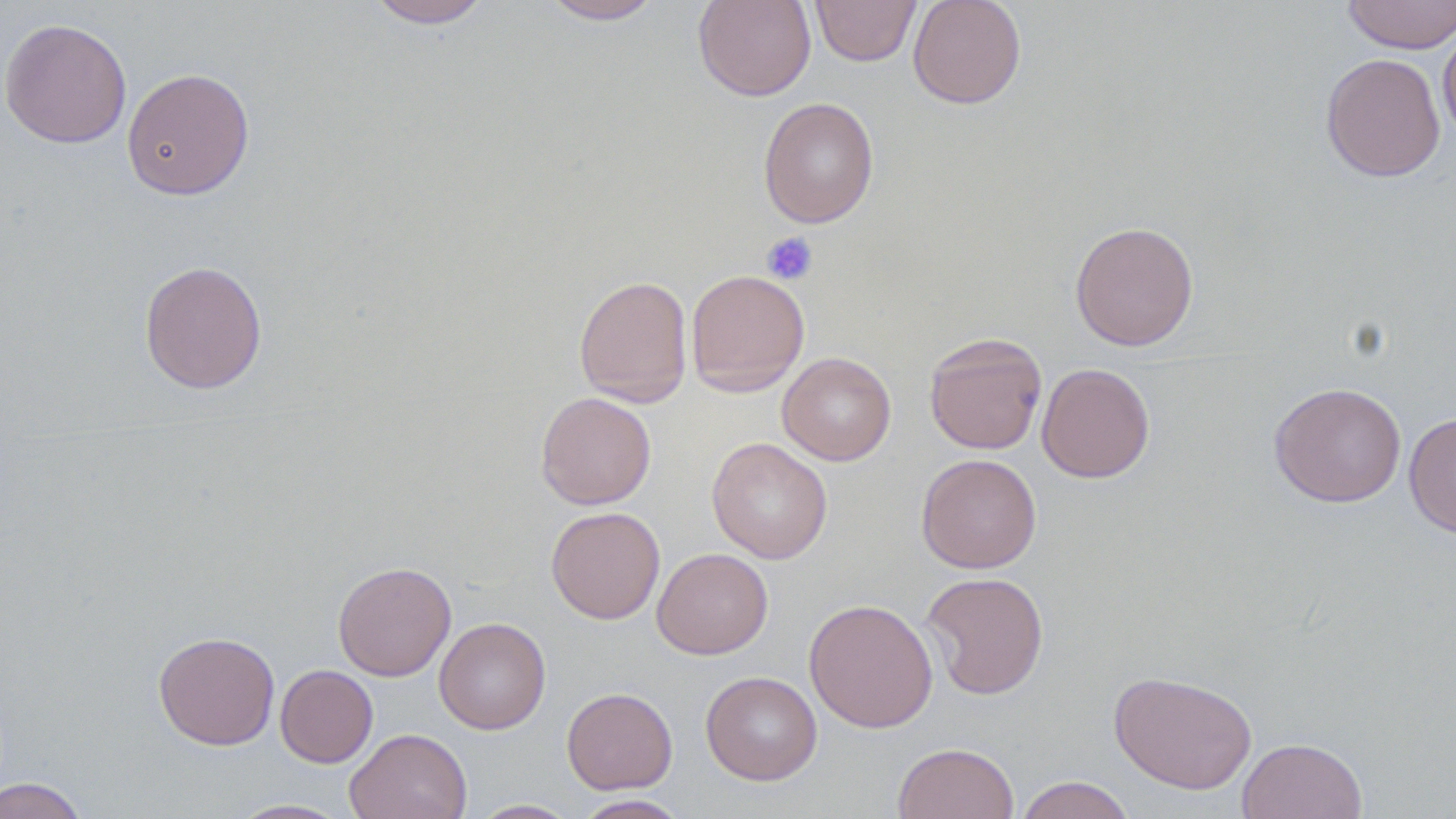 Approximate bounding boxes as named x1/y1/x2/y2 corners in pixels. Uninfected red blood cell locations: (x1=365, y1=0, x2=494, y2=28), (x1=540, y1=0, x2=665, y2=24), (x1=693, y1=0, x2=816, y2=101), (x1=810, y1=0, x2=921, y2=66), (x1=907, y1=0, x2=1027, y2=109), (x1=1341, y1=0, x2=1456, y2=54), (x1=0, y1=17, x2=132, y2=149), (x1=1438, y1=24, x2=1456, y2=144), (x1=1321, y1=52, x2=1446, y2=182), (x1=121, y1=67, x2=255, y2=200), (x1=758, y1=97, x2=879, y2=228), (x1=1070, y1=221, x2=1199, y2=351), (x1=139, y1=260, x2=268, y2=394), (x1=686, y1=269, x2=810, y2=397), (x1=574, y1=275, x2=693, y2=407), (x1=924, y1=332, x2=1048, y2=455), (x1=777, y1=352, x2=896, y2=466), (x1=1036, y1=362, x2=1155, y2=483), (x1=1268, y1=381, x2=1407, y2=508), (x1=535, y1=392, x2=656, y2=510), (x1=1404, y1=412, x2=1456, y2=539), (x1=706, y1=437, x2=833, y2=564), (x1=915, y1=453, x2=1042, y2=573), (x1=546, y1=506, x2=666, y2=624), (x1=652, y1=547, x2=773, y2=659), (x1=332, y1=561, x2=456, y2=681), (x1=920, y1=571, x2=1050, y2=699), (x1=804, y1=598, x2=938, y2=733), (x1=433, y1=616, x2=551, y2=734), (x1=152, y1=630, x2=280, y2=750), (x1=275, y1=664, x2=378, y2=767), (x1=700, y1=670, x2=822, y2=786), (x1=1109, y1=670, x2=1258, y2=794), (x1=561, y1=686, x2=677, y2=794), (x1=345, y1=728, x2=472, y2=819), (x1=1236, y1=737, x2=1368, y2=819), (x1=892, y1=742, x2=1019, y2=819), (x1=1015, y1=775, x2=1136, y2=819), (x1=0, y1=777, x2=89, y2=819), (x1=571, y1=794, x2=691, y2=818), (x1=227, y1=798, x2=353, y2=818), (x1=469, y1=799, x2=580, y2=818). Platelet locations: (x1=761, y1=232, x2=818, y2=285). Slide-level diagnosis: negative for blood parasites. 1000x magnification. May-Grünwald-Giemsa stain. Optical microscopy. Single field of view. Image is 1456×819 pixels. Thin blood smear.